Assess this cell for malaria.
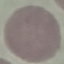

Uninfected.

Summary:
  - Stain: Giemsa
  - Image type: cell patch, automatically extracted from a larger field of view and resized to 64 × 64 pixels
  - Capture: smartphone camera at the microscope eyepiece
  - Preparation: thin blood film